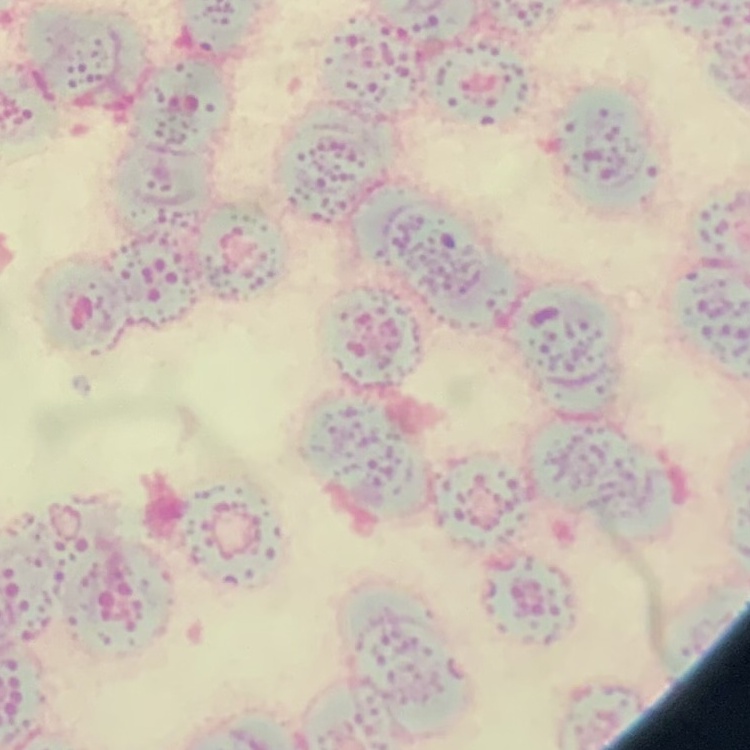

Summary:
  - Red blood cell morphology: rouleaux formation
  - Image type: one tile cut from a larger photomicrograph
  - Preparation: thin blood film
  - Stain: Field's or Giemsa